Draw a bounding box around every malaria parasite, every leukocyte, and every artifact (stain precipitate or debris).
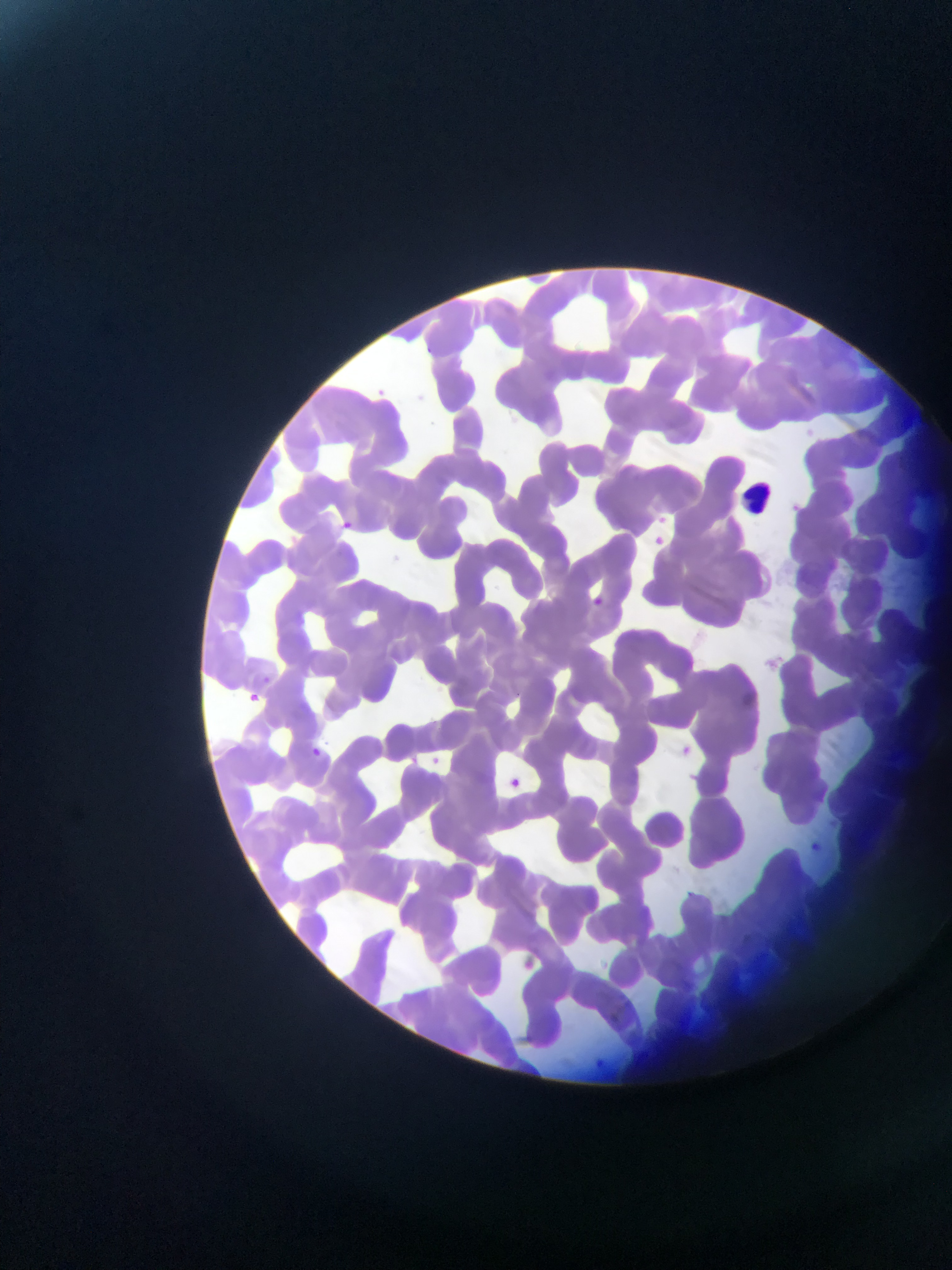
Approximate bounding boxes as (left, top, right, bottom) in pixels.
No malaria parasites observed.
Leukocytes: (744, 478, 777, 521).

image_size: 952×1270 pixels
preparation: thin blood film
country: Ghana
capture: mobile-phone photograph through a microscope
field_of_view: single